Describe the morphology of the red blood cells.
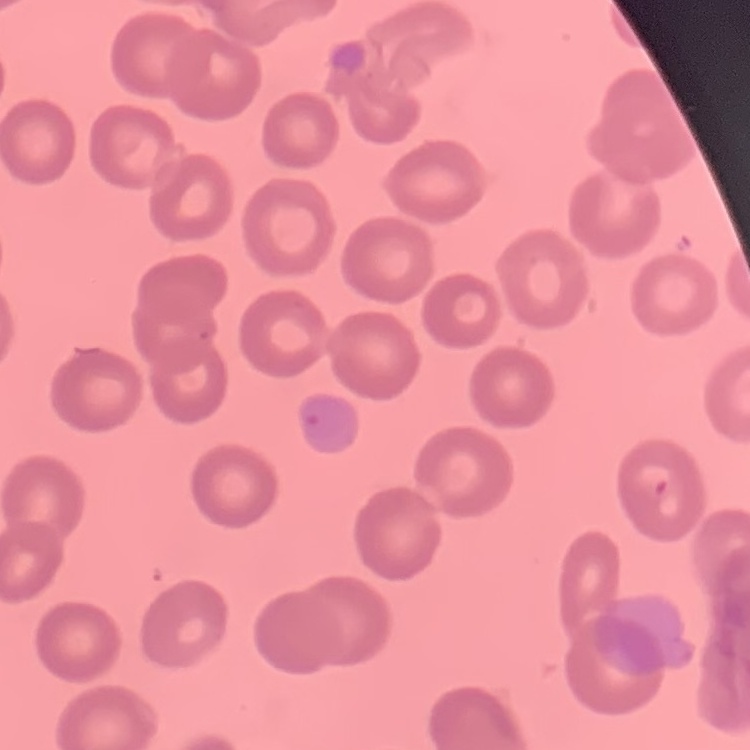

No rouleaux formation.

preparation = thin peripheral smear
stain = Field's or Giemsa
image type = one tile cut from a larger photomicrograph